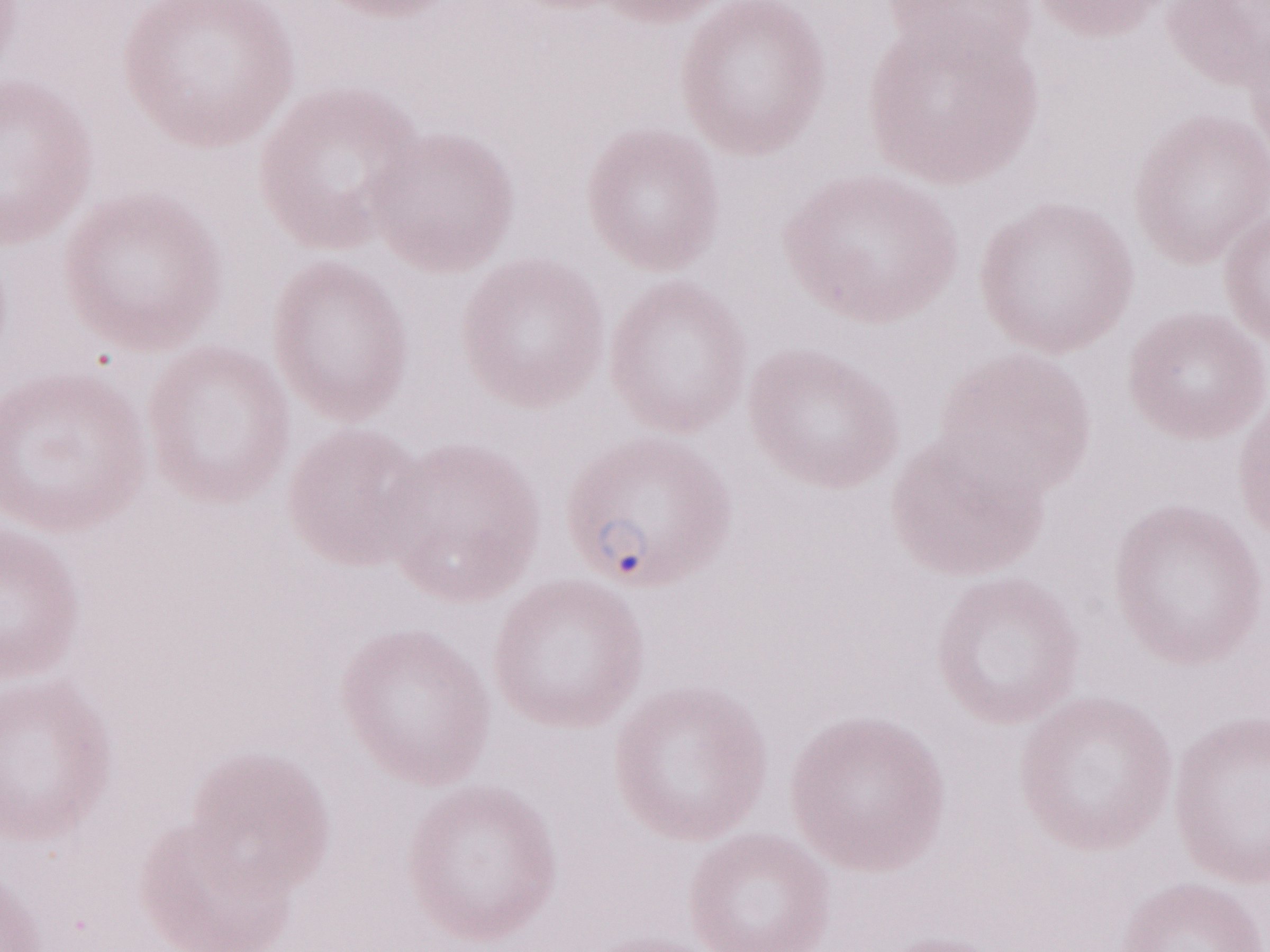

Single field of view. May-Grünwald-Giemsa-stained preparation. Malaria diagnosis (patient-level): positive. Olympus BX43 microscope and DP73 digital camera. Image is 1270×952 pixels. Thin blood smear. Magnification: 1,000x.